Classify this cell by malaria status.
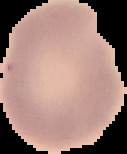

It is uninfected.

Image is 127×154 pixels. Segmented cell region on a black background. From a thin blood film.